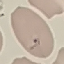

Result: malaria parasites identified. Giemsa-stained preparation. Photographed with a smartphone camera at the microscope eyepiece. Thin blood film. Cell patch, automatically extracted from a larger field of view and resized to 64 × 64 pixels.